Give the position of every leukocyte visible.
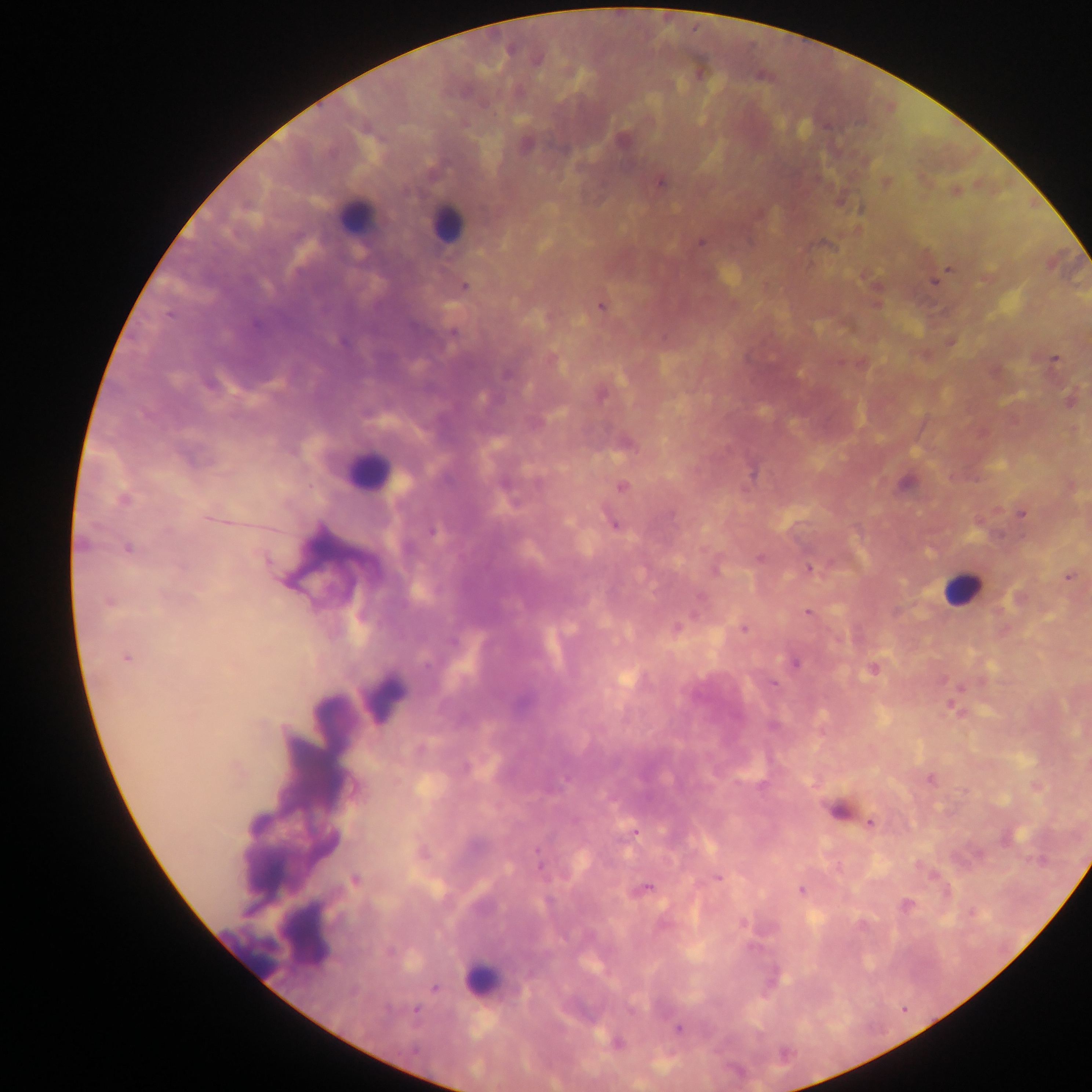

Approximate centers as x y in pixels.
Leukocytes: 352 210; 446 219; 370 470; 958 591; 482 981.

Malaria parasite locations: 623 139; 659 183; 701 241; 357 250; 948 269; 932 282; 465 284; 599 306; 1054 358; 551 360; 622 487; 122 499; 1021 512; 210 519; 612 520; 127 549; 759 556; 809 567; 1068 576; 281 579; 109 601; 698 607; 809 611; 676 627; 744 627; 127 659; 425 663; 795 663; 872 670; 774 683; 949 705; 871 822; 634 830; 716 876; 353 880; 645 890; 801 890; 906 903; 972 911; 742 923; 861 924; 679 1028. Image is 1092×1092 pixels. Thick blood film. Collected in Ghana. Single field of view. Photographed through a microscope with a mobile-phone camera.